State which parasite is depicted.
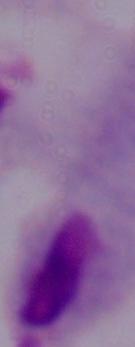

A trichomonad.

Summary:
  - Modality: micrograph
  - Magnification: 1000x